Outline each blood parasite and name the species.
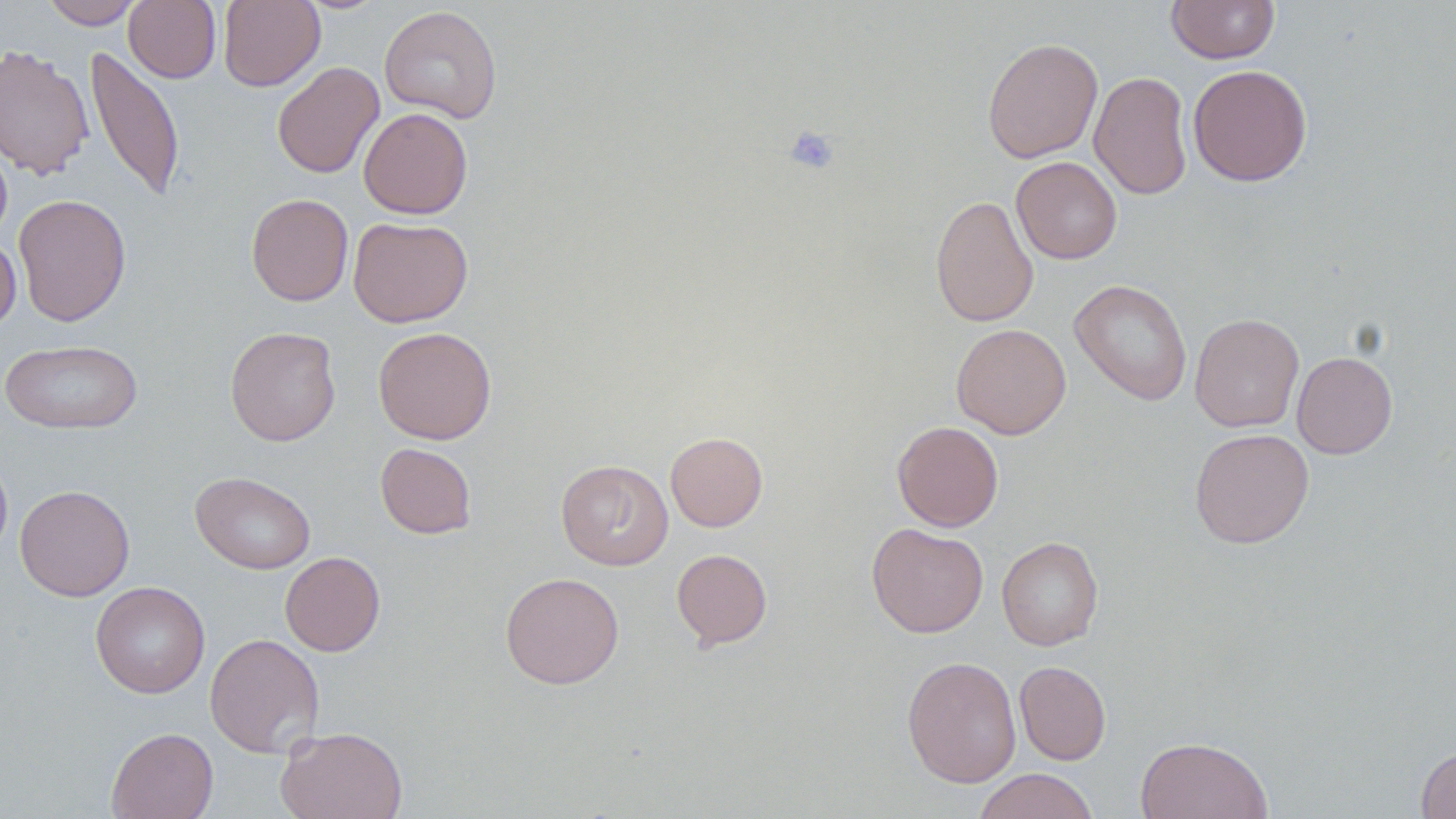
No blood parasites observed.

slide-level diagnosis = no evidence of blood parasites
preparation = thin blood film
platelet locations = approximate bounding boxes as (x1,y1)-(x2,y2) corner pairs in pixels: (784,125)-(840,175)
image size = 1456×819 pixels
stain = May-Grünwald-Giemsa
modality = light microscopy
uninfected red blood cell locations = approximate bounding boxes as (x1,y1)-(x2,y2) corner pairs in pixels: (40,0)-(143,29), (124,0)-(221,83), (218,0)-(325,91), (1165,0)-(1281,64), (379,5)-(503,124), (982,38)-(1103,163), (0,44)-(94,180), (85,46)-(185,203), (272,61)-(385,179), (1188,64)-(1312,187), (1089,70)-(1193,200), (359,107)-(473,219), (0,137)-(13,244), (1011,157)-(1122,264), (246,193)-(353,306), (13,194)-(131,326), (930,194)-(1039,328), (348,216)-(473,327), (0,234)-(21,333), (1070,279)-(1192,405), (1189,313)-(1304,433), (951,323)-(1072,439), (225,326)-(341,446), (373,326)-(496,444), (0,339)-(143,434), (1292,351)-(1398,459), (892,420)-(1004,532), (1189,428)-(1314,549), (665,431)-(768,532), (375,443)-(476,539), (0,451)-(13,561), (556,459)-(673,570), (190,471)-(315,574), (14,484)-(135,601), (866,522)-(988,638), (997,536)-(1104,650), (671,549)-(772,649), (280,551)-(385,656), (500,572)-(624,689), (90,581)-(210,698), (204,633)-(325,758), (901,656)-(1021,788), (1014,661)-(1111,765), (276,726)-(408,819), (106,727)-(218,819), (1134,736)-(1272,819), (1416,746)-(1456,818), (973,768)-(1099,819)
magnification = 1000x
field of view = one of a larger specimen